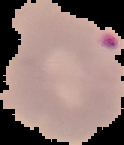
{
  "preparation": "thin blood smear",
  "result": "malaria parasites identified",
  "image_type": "segmented cell region on a black background",
  "image_size": "124×145 pixels"
}